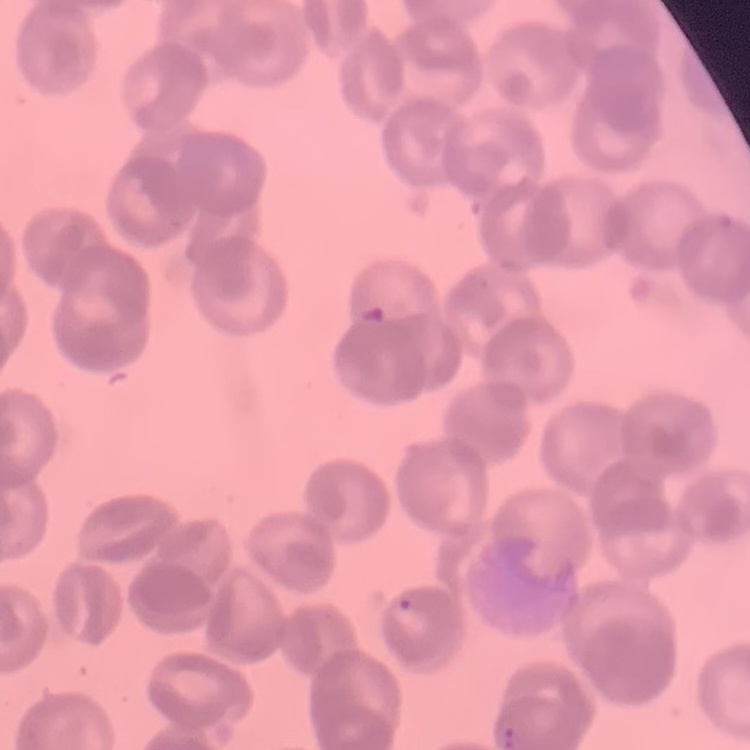

The red blood cells show rouleaux formation. Thin peripheral smear. Stained with either Field's or Giemsa. One tile cut from a larger photomicrograph.